Name the parasite shown.
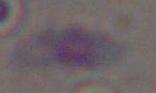

Toxoplasma gondii.

{
  "modality": "photomicrograph",
  "magnification": "1000x"
}